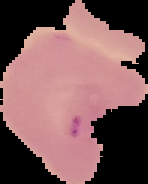
Summary:
  - Preparation: thin blood film
  - Image size: 148×184 pixels
  - Image type: cell region segmented out of the field of view; surrounding area masked to black
  - Malaria status: uninfected